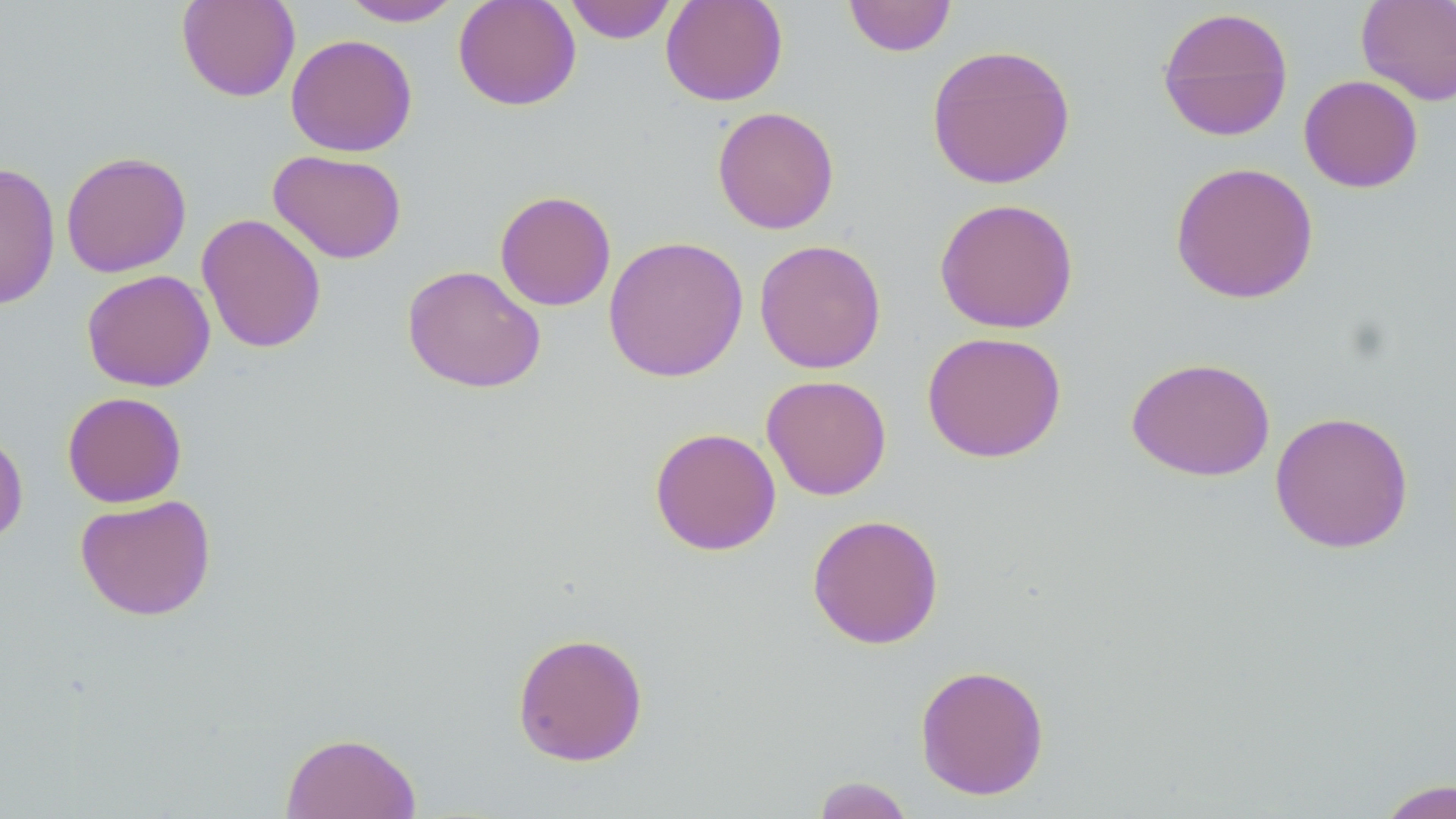

slide_level_diagnosis: negative for blood parasites
magnification: 1000x
field_of_view: one of a larger specimen
uninfected_red_blood_cell_locations: 'approximate bounding boxes as named x1/y1/x2/y2 corners in pixels: (x1=176, y1=0, x2=301, y2=102), (x1=340, y1=0, x2=463, y2=26), (x1=453, y1=0, x2=581, y2=111), (x1=660, y1=0, x2=788, y2=106), (x1=843, y1=0, x2=957, y2=57), (x1=1356, y1=0, x2=1456, y2=106), (x1=564, y1=1, x2=677, y2=44), (x1=1156, y1=6, x2=1294, y2=142), (x1=285, y1=33, x2=418, y2=157), (x1=926, y1=43, x2=1076, y2=190), (x1=1298, y1=74, x2=1423, y2=193), (x1=712, y1=106, x2=840, y2=234), (x1=268, y1=150, x2=407, y2=264), (x1=60, y1=151, x2=192, y2=278), (x1=0, y1=161, x2=61, y2=310), (x1=1169, y1=161, x2=1319, y2=304), (x1=494, y1=190, x2=616, y2=311), (x1=934, y1=197, x2=1079, y2=334), (x1=196, y1=213, x2=327, y2=354), (x1=603, y1=235, x2=749, y2=382), (x1=754, y1=239, x2=887, y2=374), (x1=402, y1=264, x2=546, y2=393), (x1=81, y1=269, x2=215, y2=392), (x1=921, y1=331, x2=1068, y2=463), (x1=1126, y1=356, x2=1275, y2=482), (x1=761, y1=374, x2=892, y2=500), (x1=61, y1=391, x2=187, y2=508), (x1=1269, y1=410, x2=1414, y2=554), (x1=0, y1=426, x2=29, y2=548), (x1=649, y1=427, x2=782, y2=556), (x1=74, y1=493, x2=217, y2=621), (x1=806, y1=513, x2=944, y2=649), (x1=511, y1=631, x2=649, y2=766), (x1=914, y1=663, x2=1050, y2=801), (x1=279, y1=731, x2=421, y2=819), (x1=812, y1=775, x2=915, y2=818), (x1=1372, y1=777, x2=1456, y2=819)'
preparation: thin blood film
stain: May-Grünwald-Giemsa
modality: optical microscopy
image_size: 1456×819 pixels